Identify the preparation type.
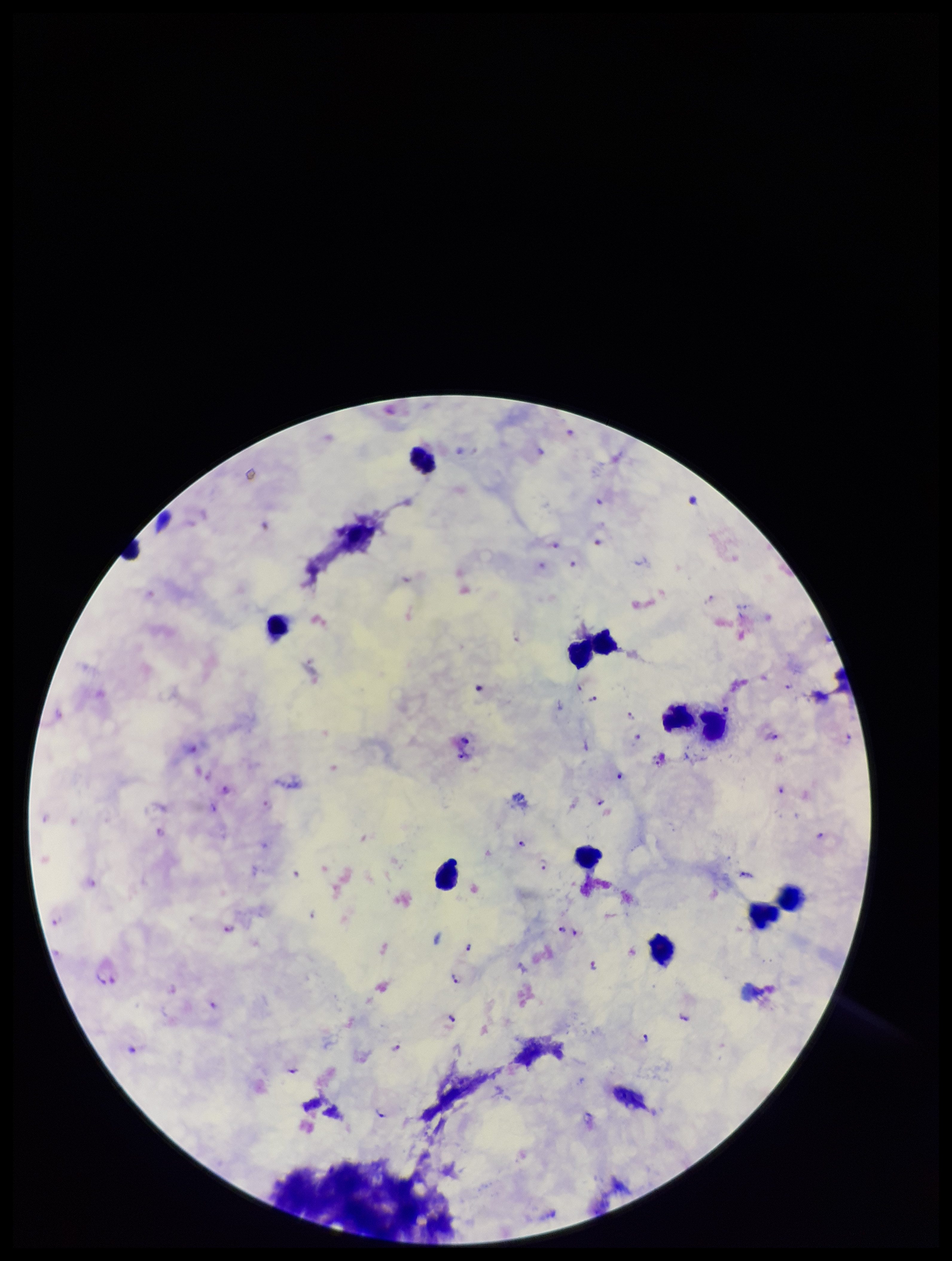

Thick.

{
  "capture": "smartphone photograph through the microscope eyepiece",
  "species_reported_for_this_patient": "Plasmodium falciparum",
  "leukocyte_count": 11,
  "parasite_count": 25,
  "field_of_view": "one from this slide",
  "image_size": "952×1261 pixels",
  "plasmodium_parasites": "seen",
  "patient_malaria_status": "positive",
  "stain": "Giemsa"
}